Identify the parasite.
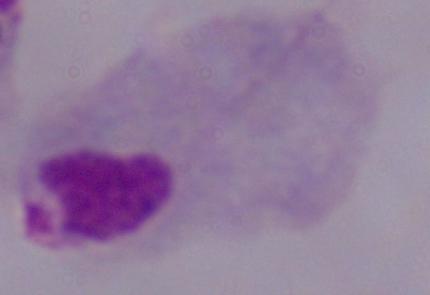

A trichomonad.

Micrograph. 1000x magnification.